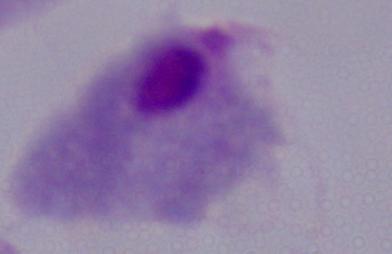

{
  "magnification": "1000x",
  "modality": "micrograph",
  "identification": "trichomonad"
}